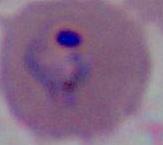

{
  "modality": "micrograph",
  "identification": "Plasmodium",
  "magnification": "400x or 1000x"
}